Classify this cell by malaria status.
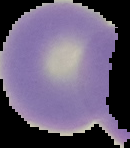
Uninfected.

From a thin blood smear. The area outside the segmented cell region is set to black. Image is 130×148 pixels.